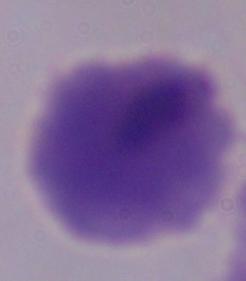

Summary:
  - Identification: trichomonad
  - Modality: photomicrograph
  - Magnification: 1000x